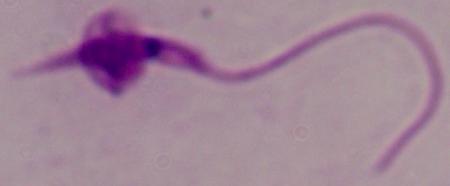 1000x magnification. Photomicrograph. A Leishmania parasite is shown.